Give the preparation type.
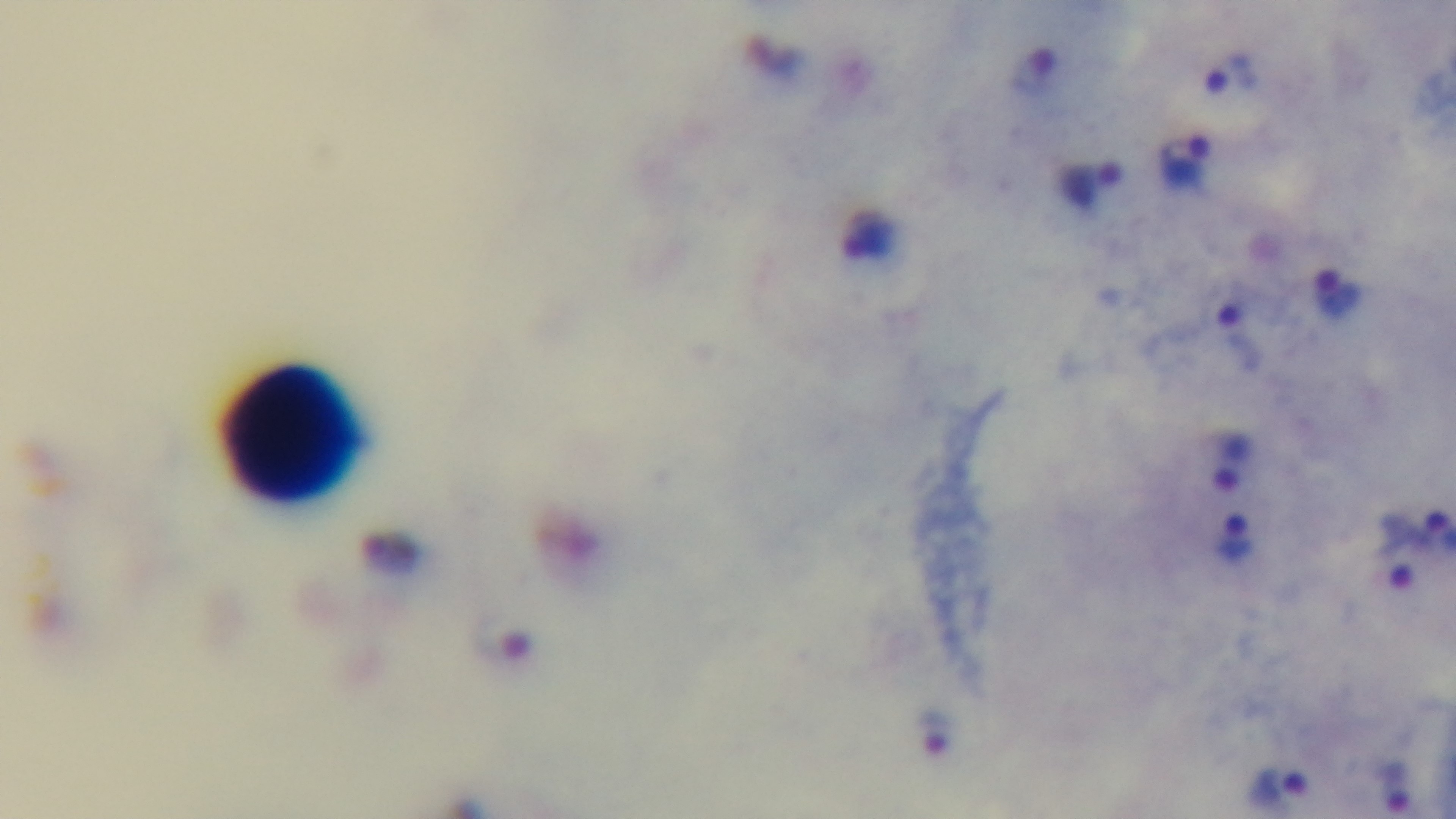

It is a thick blood film.

objective = 100x oil immersion
stain = Giemsa
modality = light microscopy
malaria status = positive
capture = mounted 4K digital camera
field of view = one from the slide